Report the malaria status of this cell.
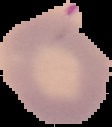
It is uninfected.

{
  "image_type": "cell region segmented out of the field of view; surrounding area masked to black",
  "preparation": "thin blood film",
  "image_size": "112×127 pixels"
}